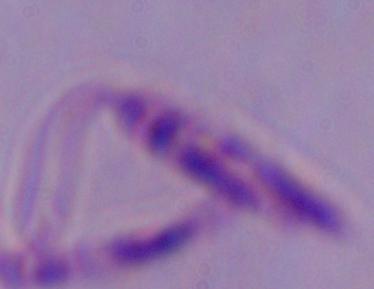

Summary:
  - Modality: micrograph
  - Magnification: 1000x
  - Identification: Leishmania